Name the cell type shown.
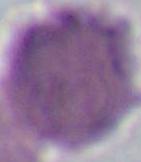

An erythrocyte.

Captured at 1000x magnification. Photomicrograph.